Locate and identify every blood parasite.
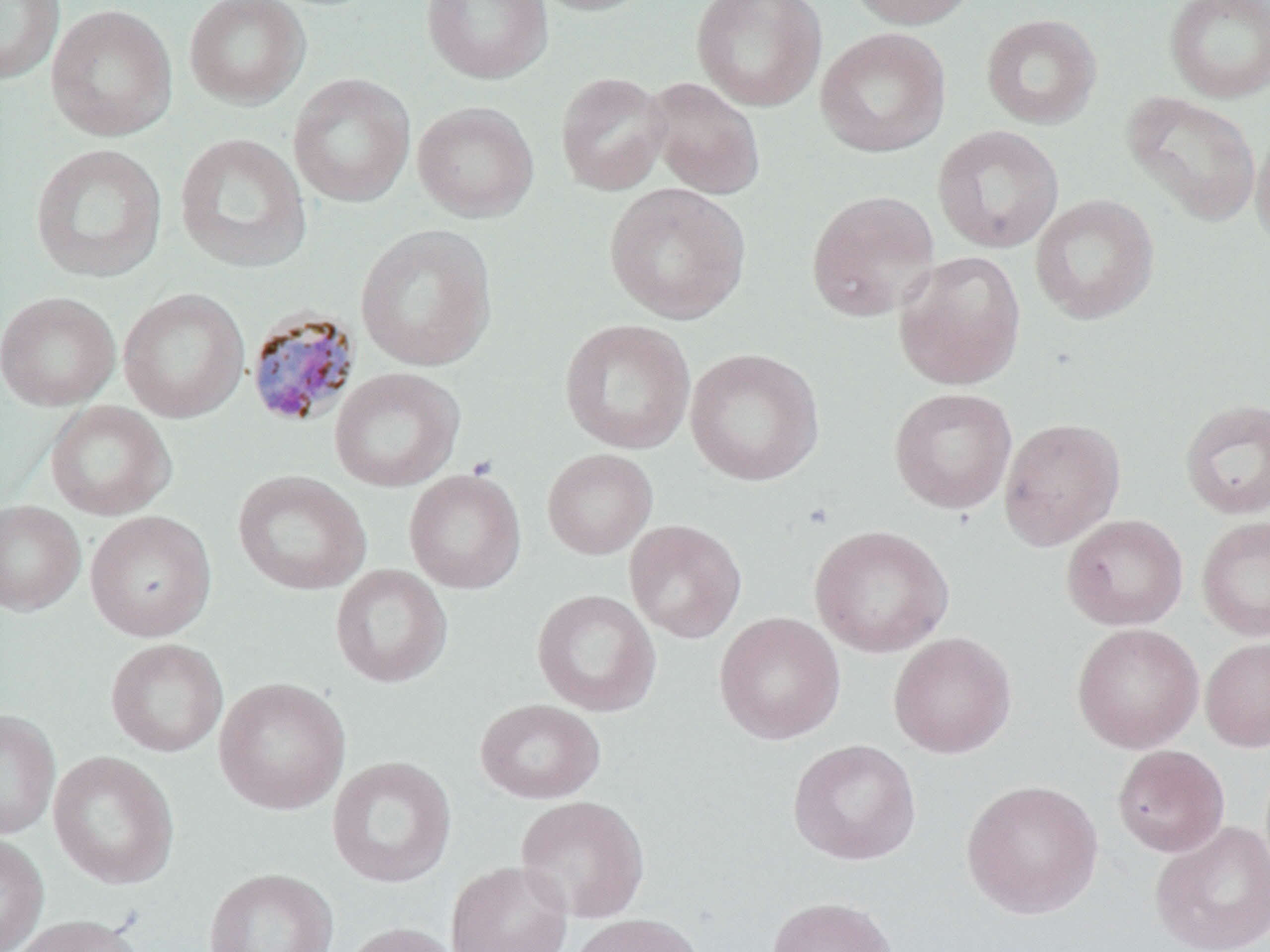
Approximate bounding boxes as (x1, y1, x2, y2) in pixels.
Plasmodium malariae-infected red blood cells: (245, 307, 362, 429).
No Plasmodium falciparum, Plasmodium ovale, Plasmodium vivax, Babesia divergens, or Trypanosoma brucei observed.

Summary:
  - Uninfected red blood cell locations: (0, 0, 64, 85), (184, 0, 311, 110), (421, 0, 553, 85), (526, 0, 657, 16), (691, 0, 826, 111), (844, 0, 982, 29), (1164, 0, 1270, 103), (46, 4, 178, 142), (981, 13, 1102, 129), (816, 27, 951, 158), (555, 71, 671, 195), (288, 73, 416, 208), (644, 78, 765, 199), (1122, 91, 1261, 226), (412, 101, 539, 222), (1251, 123, 1270, 255), (933, 125, 1064, 253), (174, 132, 311, 273), (30, 143, 167, 283), (604, 183, 751, 324), (806, 190, 940, 321), (1030, 194, 1159, 325), (354, 224, 497, 372), (893, 251, 1026, 390), (118, 287, 250, 423), (0, 291, 121, 411), (559, 319, 696, 454), (685, 348, 825, 486), (329, 367, 465, 492), (889, 387, 1017, 514), (1179, 398, 1270, 520), (45, 400, 176, 521), (998, 417, 1126, 550), (542, 449, 658, 559), (404, 469, 526, 594), (232, 470, 371, 595), (0, 500, 86, 616), (85, 510, 216, 642), (1061, 514, 1188, 631), (1196, 516, 1270, 641), (624, 519, 747, 643), (810, 524, 953, 658), (330, 564, 453, 688), (532, 589, 661, 717), (713, 611, 846, 745), (1072, 623, 1204, 753), (888, 631, 1016, 758), (1200, 636, 1270, 752), (105, 638, 228, 757), (213, 678, 351, 815), (475, 698, 605, 804), (0, 709, 60, 840), (788, 739, 921, 865), (1112, 744, 1230, 857), (48, 750, 180, 889), (327, 756, 457, 888), (961, 779, 1104, 918), (515, 795, 650, 923), (1149, 820, 1270, 952), (0, 833, 49, 952), (446, 860, 573, 952), (203, 868, 339, 952), (766, 895, 898, 952), (567, 913, 706, 952), (8, 914, 145, 952), (337, 921, 464, 952)
  - Slide-level diagnosis: Plasmodium malariae
  - Image size: 1270×952 pixels
  - Preparation: thin blood smear
  - Modality: light microscopy
  - Stain: May-Grünwald-Giemsa
  - Field of view: one of a larger specimen
  - Magnification: 1000x